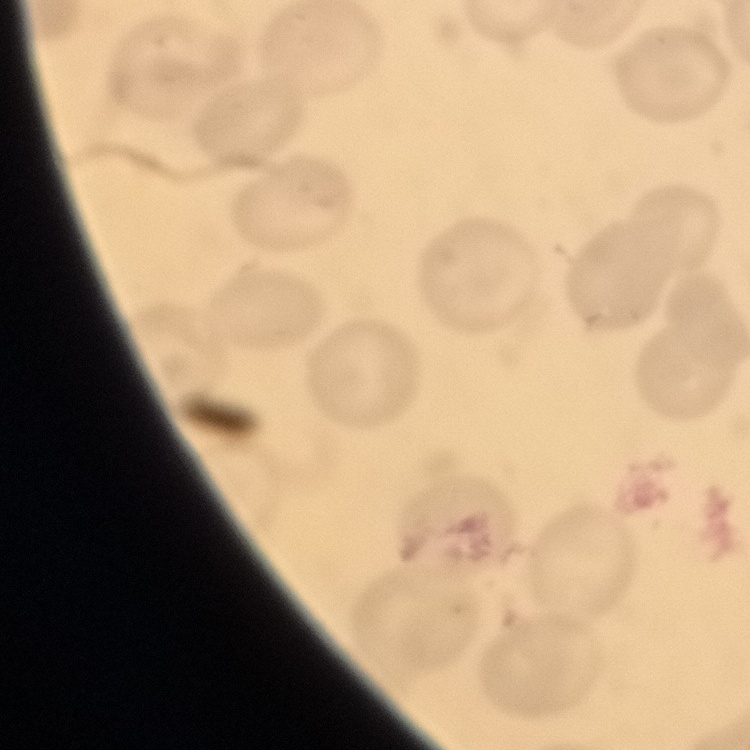
{
  "erythrocyte_morphology": "no rouleaux formation",
  "preparation": "thin peripheral smear",
  "image_type": "square crop of a larger photomicrograph",
  "stain": "Field's or Giemsa"
}